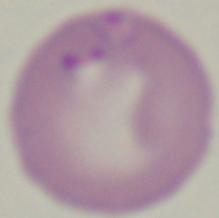
modality: micrograph
identification: Babesia
magnification: 1000x